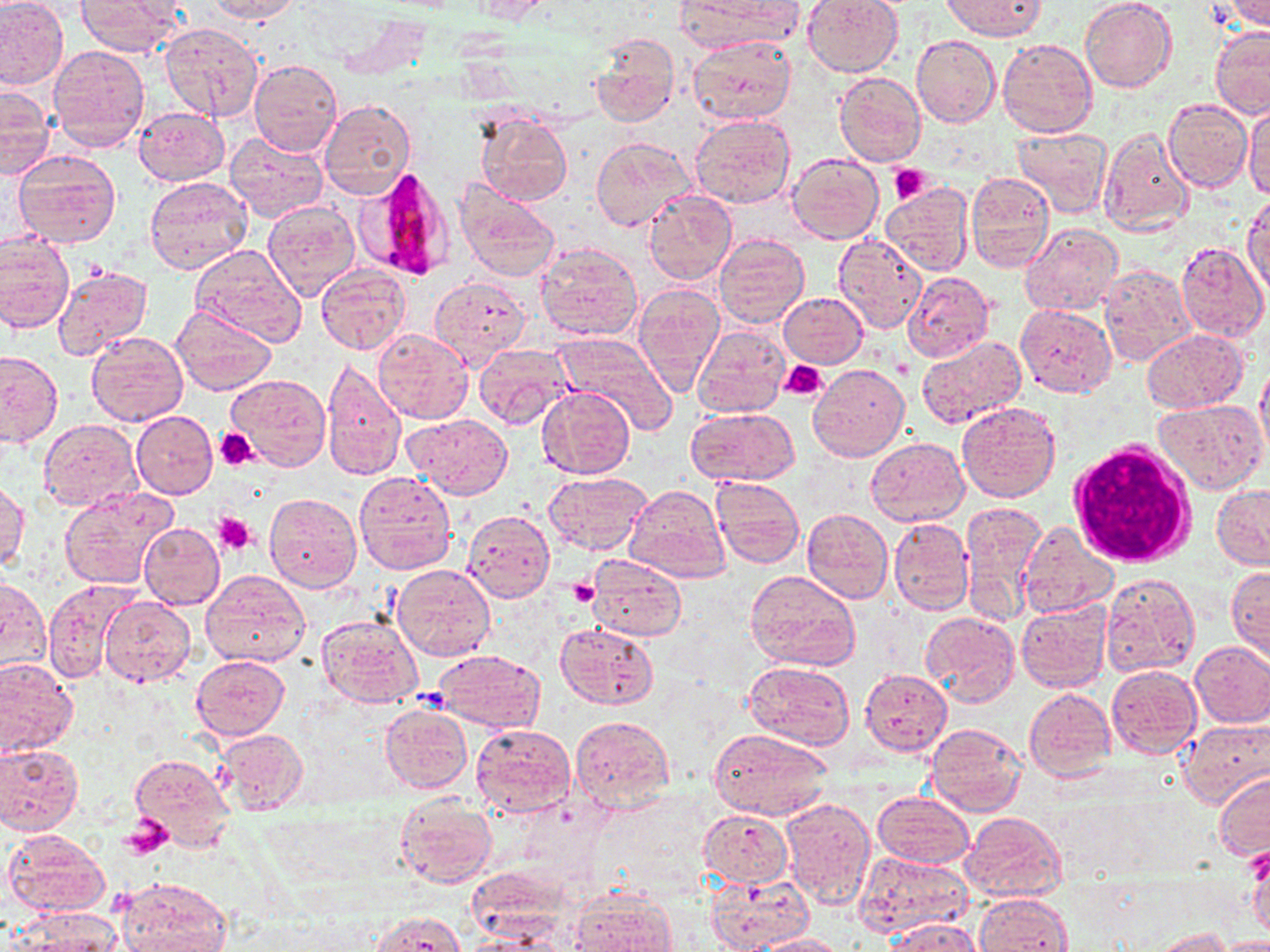

Approximate bounding boxes as named x1/y1/x2/y2 corners in pixels. White blood cell locations: (x1=1070, y1=439, x2=1198, y2=565). Uninfected red blood cell locations: (x1=204, y1=0, x2=301, y2=23), (x1=470, y1=0, x2=547, y2=23), (x1=682, y1=0, x2=796, y2=54), (x1=801, y1=0, x2=904, y2=77), (x1=941, y1=0, x2=1046, y2=41), (x1=1080, y1=0, x2=1176, y2=94), (x1=0, y1=1, x2=67, y2=90), (x1=74, y1=1, x2=185, y2=55), (x1=1225, y1=1, x2=1269, y2=31), (x1=161, y1=22, x2=264, y2=121), (x1=1209, y1=26, x2=1270, y2=119), (x1=590, y1=33, x2=678, y2=127), (x1=912, y1=35, x2=1000, y2=128), (x1=687, y1=36, x2=797, y2=125), (x1=997, y1=38, x2=1097, y2=139), (x1=48, y1=45, x2=149, y2=151), (x1=249, y1=58, x2=342, y2=156), (x1=835, y1=72, x2=926, y2=167), (x1=0, y1=85, x2=53, y2=179), (x1=1164, y1=99, x2=1252, y2=191), (x1=318, y1=100, x2=416, y2=201), (x1=1243, y1=103, x2=1270, y2=198), (x1=134, y1=106, x2=228, y2=185), (x1=477, y1=113, x2=572, y2=206), (x1=690, y1=114, x2=796, y2=208), (x1=1099, y1=125, x2=1194, y2=236), (x1=1012, y1=128, x2=1112, y2=219), (x1=224, y1=132, x2=329, y2=223), (x1=591, y1=135, x2=694, y2=231), (x1=13, y1=149, x2=121, y2=249), (x1=787, y1=152, x2=882, y2=243), (x1=965, y1=172, x2=1055, y2=273), (x1=143, y1=175, x2=253, y2=274), (x1=454, y1=180, x2=561, y2=281), (x1=884, y1=182, x2=973, y2=278), (x1=645, y1=191, x2=737, y2=285), (x1=1244, y1=192, x2=1270, y2=298), (x1=263, y1=200, x2=360, y2=300), (x1=1021, y1=221, x2=1123, y2=315), (x1=0, y1=232, x2=73, y2=334), (x1=715, y1=233, x2=810, y2=329), (x1=832, y1=235, x2=927, y2=335), (x1=535, y1=242, x2=645, y2=342), (x1=1174, y1=242, x2=1269, y2=340), (x1=189, y1=246, x2=306, y2=344), (x1=315, y1=263, x2=411, y2=355), (x1=1098, y1=264, x2=1196, y2=366), (x1=52, y1=265, x2=154, y2=359), (x1=903, y1=272, x2=993, y2=363), (x1=429, y1=275, x2=532, y2=366), (x1=633, y1=283, x2=725, y2=396), (x1=780, y1=293, x2=866, y2=368), (x1=171, y1=302, x2=277, y2=396), (x1=1015, y1=304, x2=1117, y2=397), (x1=693, y1=324, x2=790, y2=419), (x1=373, y1=327, x2=473, y2=424), (x1=1142, y1=328, x2=1249, y2=413), (x1=85, y1=331, x2=188, y2=425), (x1=554, y1=332, x2=678, y2=433), (x1=916, y1=335, x2=1027, y2=428), (x1=475, y1=344, x2=575, y2=429), (x1=0, y1=351, x2=62, y2=447), (x1=323, y1=357, x2=407, y2=481), (x1=1255, y1=360, x2=1270, y2=461), (x1=808, y1=364, x2=909, y2=461), (x1=226, y1=374, x2=332, y2=469), (x1=537, y1=386, x2=635, y2=480), (x1=1155, y1=397, x2=1267, y2=494), (x1=957, y1=402, x2=1062, y2=502), (x1=686, y1=407, x2=797, y2=486), (x1=132, y1=410, x2=217, y2=499), (x1=403, y1=413, x2=512, y2=499), (x1=39, y1=420, x2=141, y2=512), (x1=864, y1=436, x2=968, y2=525), (x1=353, y1=471, x2=456, y2=575), (x1=542, y1=471, x2=652, y2=554), (x1=711, y1=475, x2=804, y2=569), (x1=1, y1=481, x2=30, y2=574), (x1=624, y1=484, x2=731, y2=581), (x1=1212, y1=485, x2=1270, y2=570), (x1=59, y1=487, x2=178, y2=590), (x1=264, y1=494, x2=361, y2=593), (x1=960, y1=500, x2=1046, y2=627), (x1=802, y1=509, x2=893, y2=604), (x1=463, y1=510, x2=554, y2=602), (x1=889, y1=518, x2=973, y2=614), (x1=1019, y1=522, x2=1118, y2=618), (x1=138, y1=523, x2=225, y2=609), (x1=588, y1=554, x2=686, y2=642), (x1=391, y1=565, x2=494, y2=662), (x1=1227, y1=566, x2=1269, y2=661), (x1=201, y1=569, x2=311, y2=667), (x1=746, y1=570, x2=860, y2=674), (x1=1100, y1=572, x2=1201, y2=677), (x1=0, y1=575, x2=50, y2=677), (x1=43, y1=579, x2=139, y2=683), (x1=100, y1=595, x2=196, y2=686), (x1=1017, y1=601, x2=1111, y2=693), (x1=922, y1=612, x2=1021, y2=708), (x1=317, y1=615, x2=423, y2=708), (x1=555, y1=622, x2=658, y2=710), (x1=1189, y1=641, x2=1270, y2=727), (x1=434, y1=649, x2=545, y2=731), (x1=191, y1=655, x2=290, y2=739), (x1=0, y1=657, x2=78, y2=757), (x1=743, y1=661, x2=855, y2=751), (x1=1105, y1=664, x2=1201, y2=759), (x1=861, y1=669, x2=951, y2=754), (x1=1024, y1=688, x2=1116, y2=781), (x1=379, y1=704, x2=471, y2=794), (x1=570, y1=715, x2=676, y2=812), (x1=1179, y1=719, x2=1270, y2=807), (x1=926, y1=723, x2=1026, y2=816), (x1=470, y1=724, x2=577, y2=818), (x1=213, y1=729, x2=309, y2=818), (x1=708, y1=729, x2=830, y2=814), (x1=0, y1=744, x2=83, y2=835), (x1=131, y1=752, x2=234, y2=851), (x1=1214, y1=770, x2=1270, y2=861), (x1=873, y1=792, x2=975, y2=869), (x1=395, y1=795, x2=497, y2=888), (x1=780, y1=795, x2=877, y2=909), (x1=868, y1=801, x2=1057, y2=882), (x1=698, y1=809, x2=792, y2=889), (x1=959, y1=812, x2=1067, y2=902), (x1=2, y1=829, x2=111, y2=918), (x1=1245, y1=838, x2=1270, y2=937), (x1=855, y1=851, x2=974, y2=937), (x1=705, y1=873, x2=813, y2=952), (x1=118, y1=877, x2=232, y2=952), (x1=569, y1=891, x2=677, y2=952), (x1=974, y1=893, x2=1072, y2=952), (x1=14, y1=908, x2=124, y2=952), (x1=371, y1=911, x2=469, y2=952), (x1=887, y1=918, x2=983, y2=952), (x1=1155, y1=928, x2=1231, y2=952), (x1=750, y1=934, x2=849, y2=952), (x1=1215, y1=937, x2=1270, y2=952). Plasmodium falciparum-infected red blood cell locations: (x1=357, y1=166, x2=456, y2=282). Platelet locations: (x1=890, y1=164, x2=931, y2=205), (x1=780, y1=360, x2=828, y2=400), (x1=215, y1=428, x2=258, y2=471), (x1=213, y1=513, x2=255, y2=554), (x1=570, y1=580, x2=597, y2=604), (x1=122, y1=816, x2=172, y2=859). Slide-level diagnosis: Plasmodium falciparum. Image is 1270×952 pixels. Thin blood film. Captured at 1000x magnification. May-Grünwald-Giemsa-stained preparation. One field of a larger specimen. Optical microscopy.